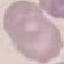
result = negative for malaria parasites
capture = smartphone through the microscope eyepiece
preparation = thin smear
stain = Giemsa
image type = automatically extracted cell patch, resized to 64 × 64 pixels